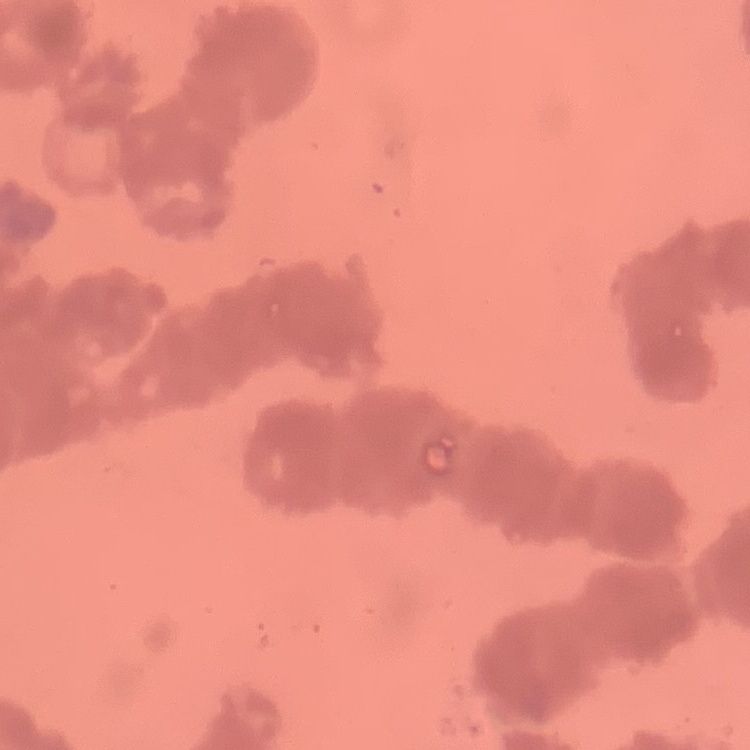
Summary:
  - Erythrocyte morphology: rouleaux formation
  - Image type: square crop of a larger photomicrograph
  - Stain: Field's or Giemsa
  - Preparation: thin peripheral smear